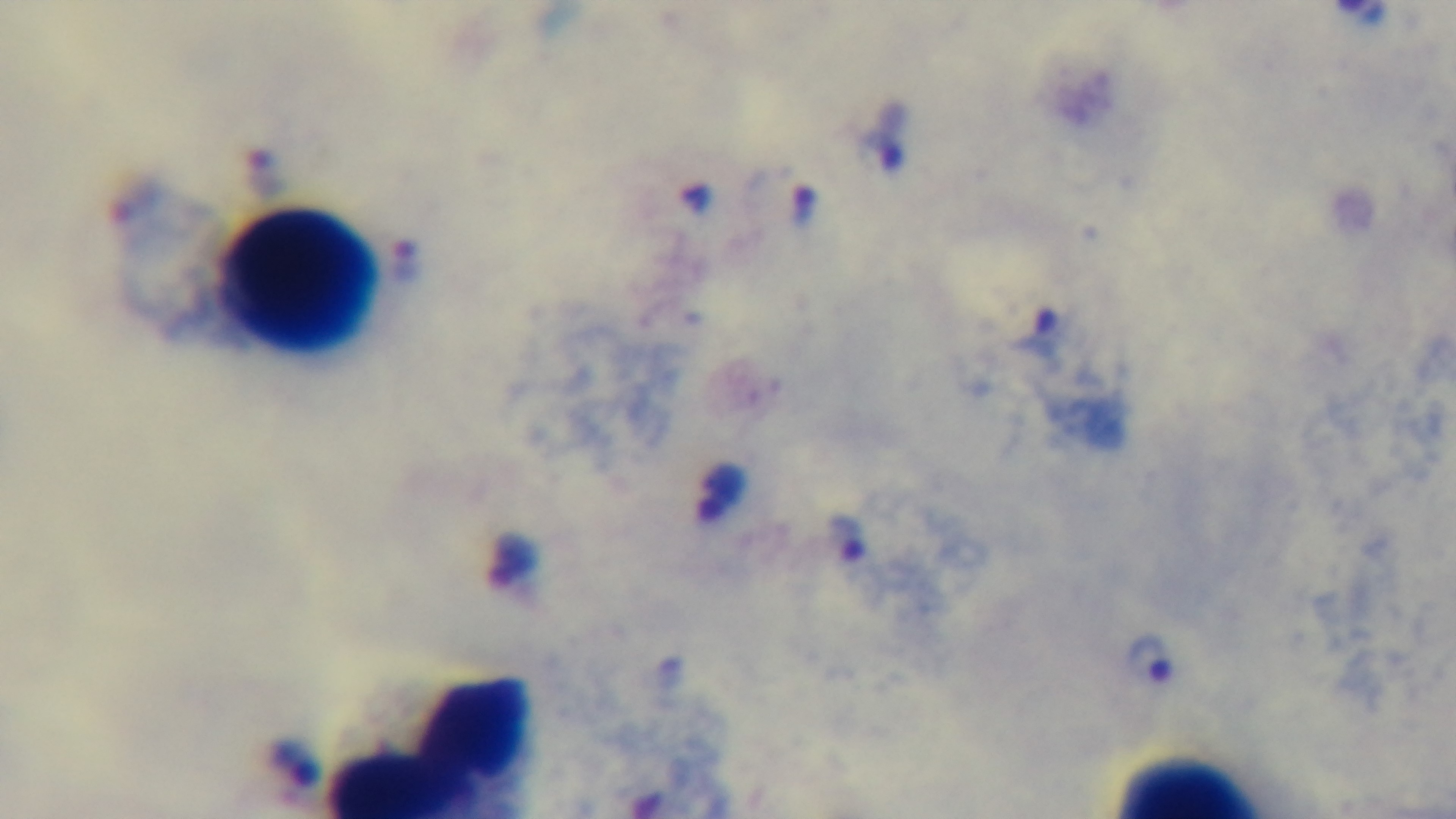
Summary:
  - Field of view: one from the slide
  - Stain: Giemsa
  - Modality: light microscopy
  - Capture: mounted 4K digital camera
  - Malaria status: infected
  - Preparation: thick blood film
  - Objective: 100x oil immersion